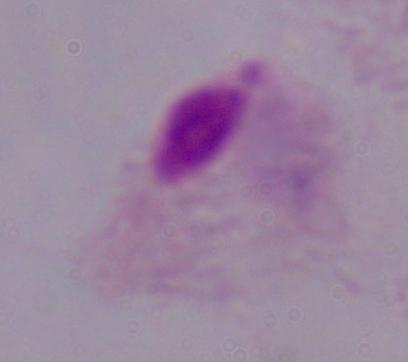

{
  "magnification": "1000x",
  "identification": "trichomonad",
  "modality": "micrograph"
}